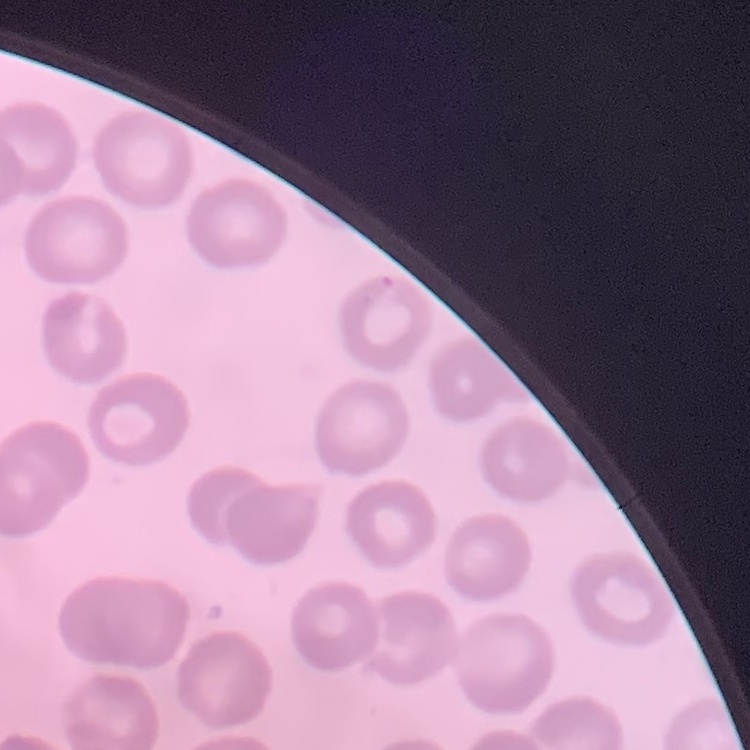
red blood cell morphology = no rouleaux formation
stain = Field's or Giemsa
preparation = thin blood film
image type = one tile cut from a larger photomicrograph